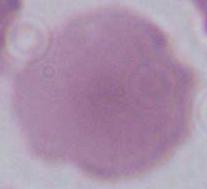

Summary:
  - Identification: red blood cell
  - Modality: photomicrograph
  - Magnification: 1000x